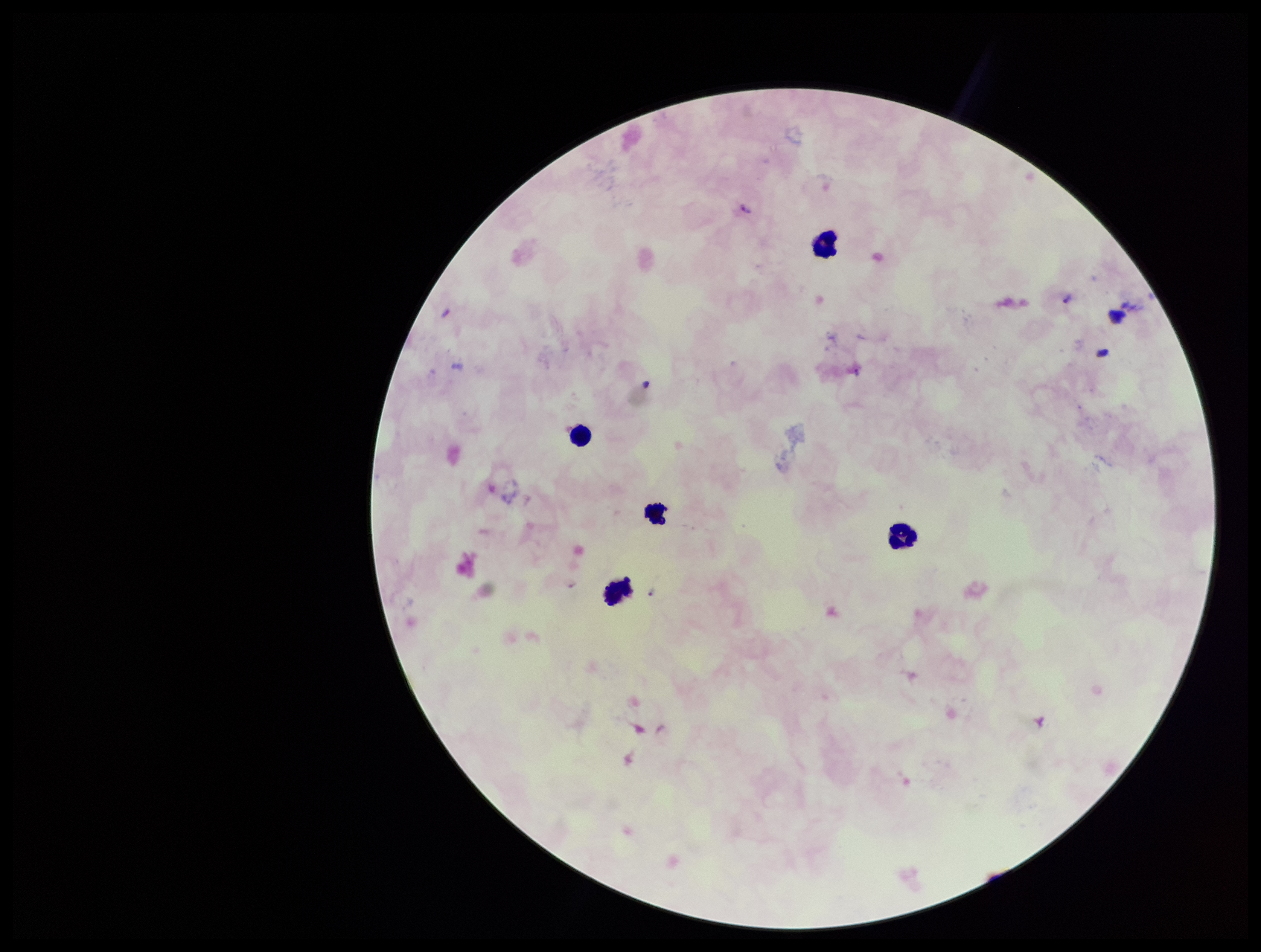
preparation: thick blood smear
leukocyte_count: 5
plasmodium_parasites: detected
patient_malaria_status: positive
stain: Giemsa
capture: smartphone photograph through the microscope eyepiece
species_reported_for_this_patient: Plasmodium falciparum
field_of_view: single
parasite_count: 3
image_size: 1261×952 pixels